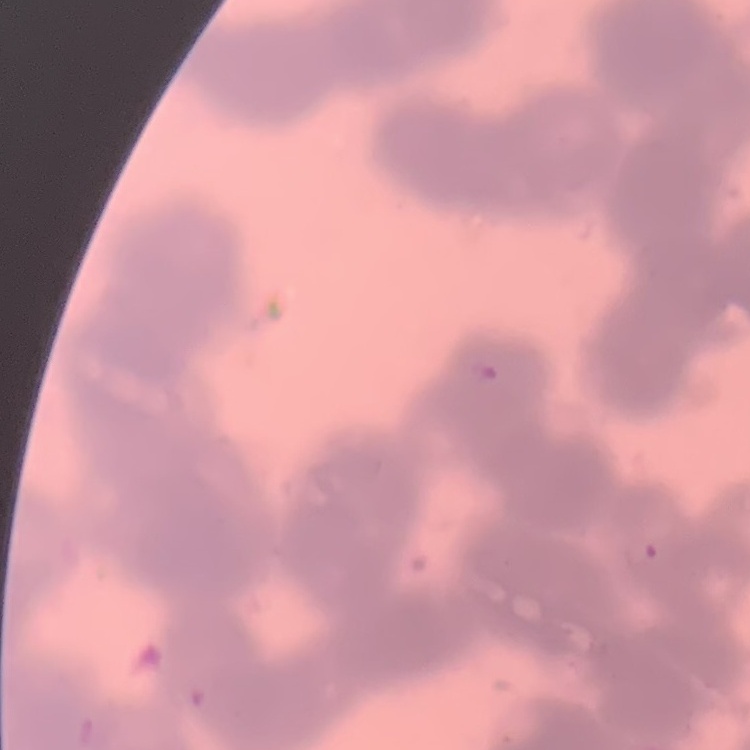 The red blood cells show rouleaux formation. One tile cut from a larger photomicrograph. Thin blood film. Stained with either Field's or Giemsa.